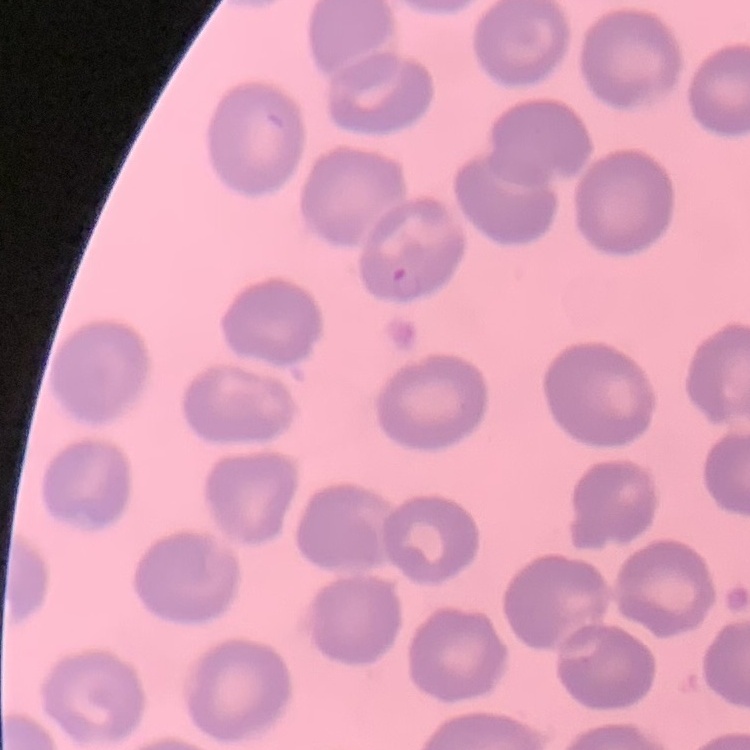

Summary:
  - Red blood cell morphology: no rouleaux formation
  - Image type: one tile cut from a larger photomicrograph
  - Stain: Field's or Giemsa
  - Preparation: thin blood smear